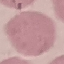

Summary:
  - Result: no malaria parasites seen
  - Capture: smartphone camera at the microscope eyepiece
  - Preparation: thin blood smear
  - Stain: Giemsa
  - Image type: cell patch, automatically extracted from a larger field of view and resized to 64 × 64 pixels